Report the malaria status of this cell.
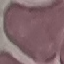

It is uninfected.

{
  "image_type": "cell patch, automatically extracted from a larger field of view and resized to 64 × 64 pixels",
  "preparation": "thin smear",
  "capture": "smartphone through the microscope eyepiece",
  "stain": "Giemsa"
}